Classify this cell by malaria status.
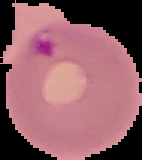
It is parasitized.

image size = 142×160 pixels
preparation = thin blood film
image type = cell region segmented out of the field of view; surrounding area masked to black